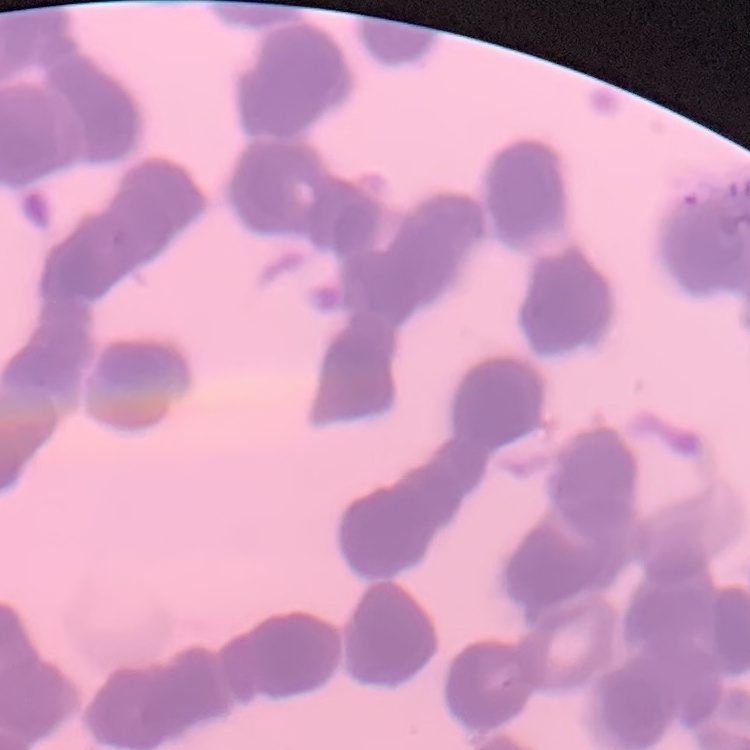

Summary:
  - Erythrocyte morphology: rouleaux formation
  - Stain: Field's or Giemsa
  - Image type: one tile cut from a larger photomicrograph
  - Preparation: thin peripheral smear